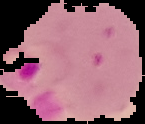
{
  "preparation": "thin blood smear",
  "image_size": "145×124 pixels",
  "malaria_status": "parasitized",
  "image_type": "segmented cell region on a black background"
}